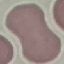
Result: no malaria parasites detected. Photographed with a smartphone camera at the microscope eyepiece. Giemsa-stained preparation. Thin blood film. Cell patch, automatically extracted from a larger field of view and resized to 64 × 64 pixels.